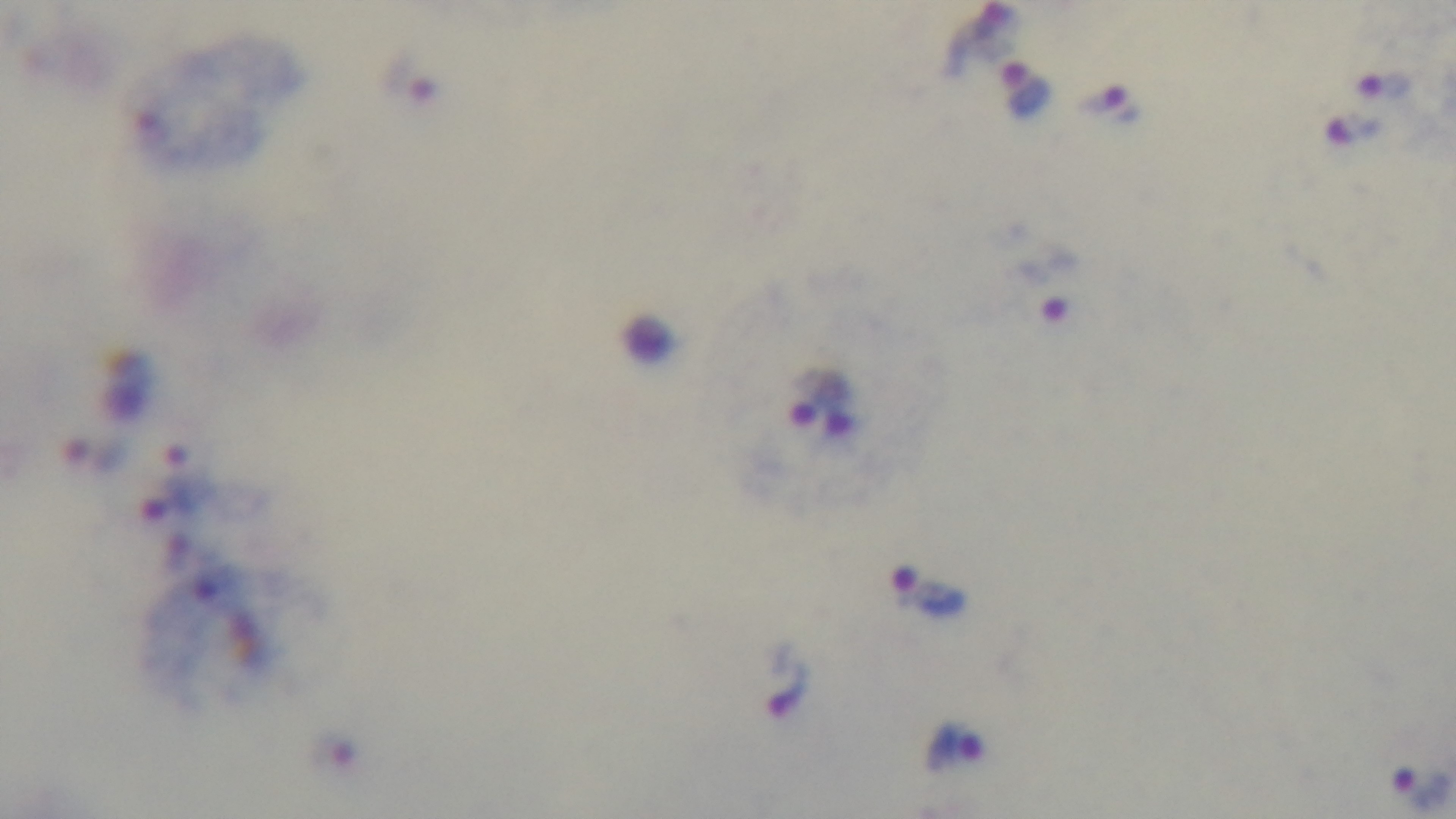

objective = 100x oil immersion
stain = Giemsa
capture = mounted 4K digital camera
modality = light microscopy
field of view = one from the slide
malaria status = positive
preparation = thick smear